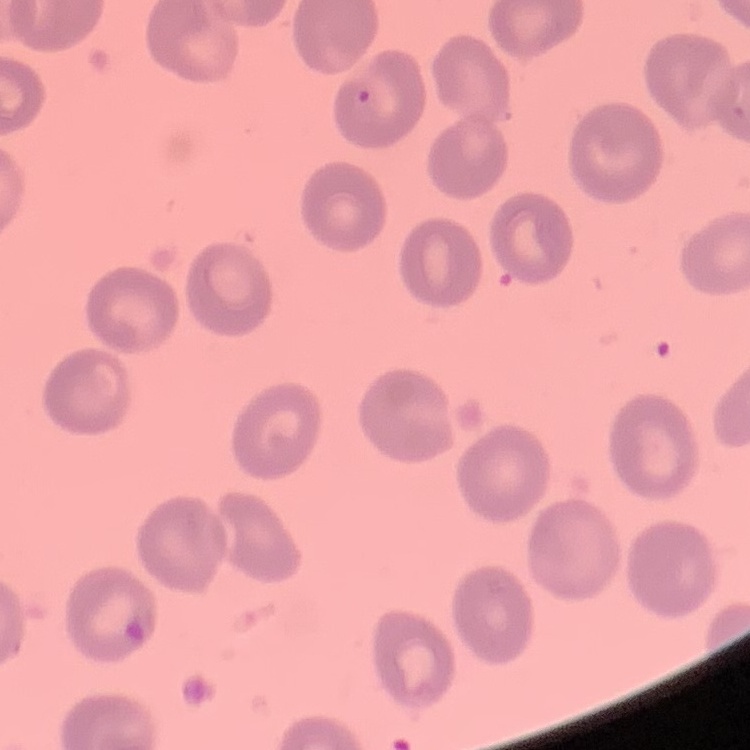

The erythrocytes exhibit no rouleaux formation. One tile cut from a larger photomicrograph. Thin blood film. Stained with either Field's or Giemsa.